Report the malaria status of this cell.
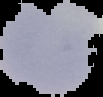

It is uninfected.

preparation = thin blood smear
image size = 103×97 pixels
image type = segmented cell region on a black background